Report the malaria status of this cell.
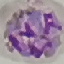

Parasitized.

Summary:
  - Capture: smartphone through the microscope eyepiece
  - Image type: automatically extracted cell patch, resized to 64 × 64 pixels
  - Preparation: thin blood smear
  - Stain: Giemsa